Name the cell type shown.
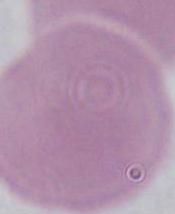

An erythrocyte.

Captured at 1000x magnification. Micrograph.